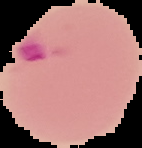

Summary:
  - Image size: 142×148 pixels
  - Preparation: thin blood film
  - Image type: segmented cell region on a black background
  - Malaria status: parasitized